Name the cell type shown.
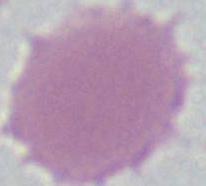
An erythrocyte.

magnification = 1000x
modality = micrograph